Classify this cell by malaria status.
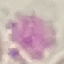

It is uninfected.

Summary:
  - Image type: automatically extracted cell patch, resized to 64 × 64 pixels
  - Capture: smartphone camera at the microscope eyepiece
  - Stain: Giemsa
  - Preparation: thin smear